Classify this cell by malaria status.
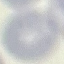

It is uninfected.

Summary:
  - Capture: smartphone through the microscope eyepiece
  - Image type: automatically extracted cell patch, resized to 64 × 64 pixels
  - Preparation: thin blood film
  - Stain: Giemsa